Outline each Plasmodium ovale-infected red blood cell.
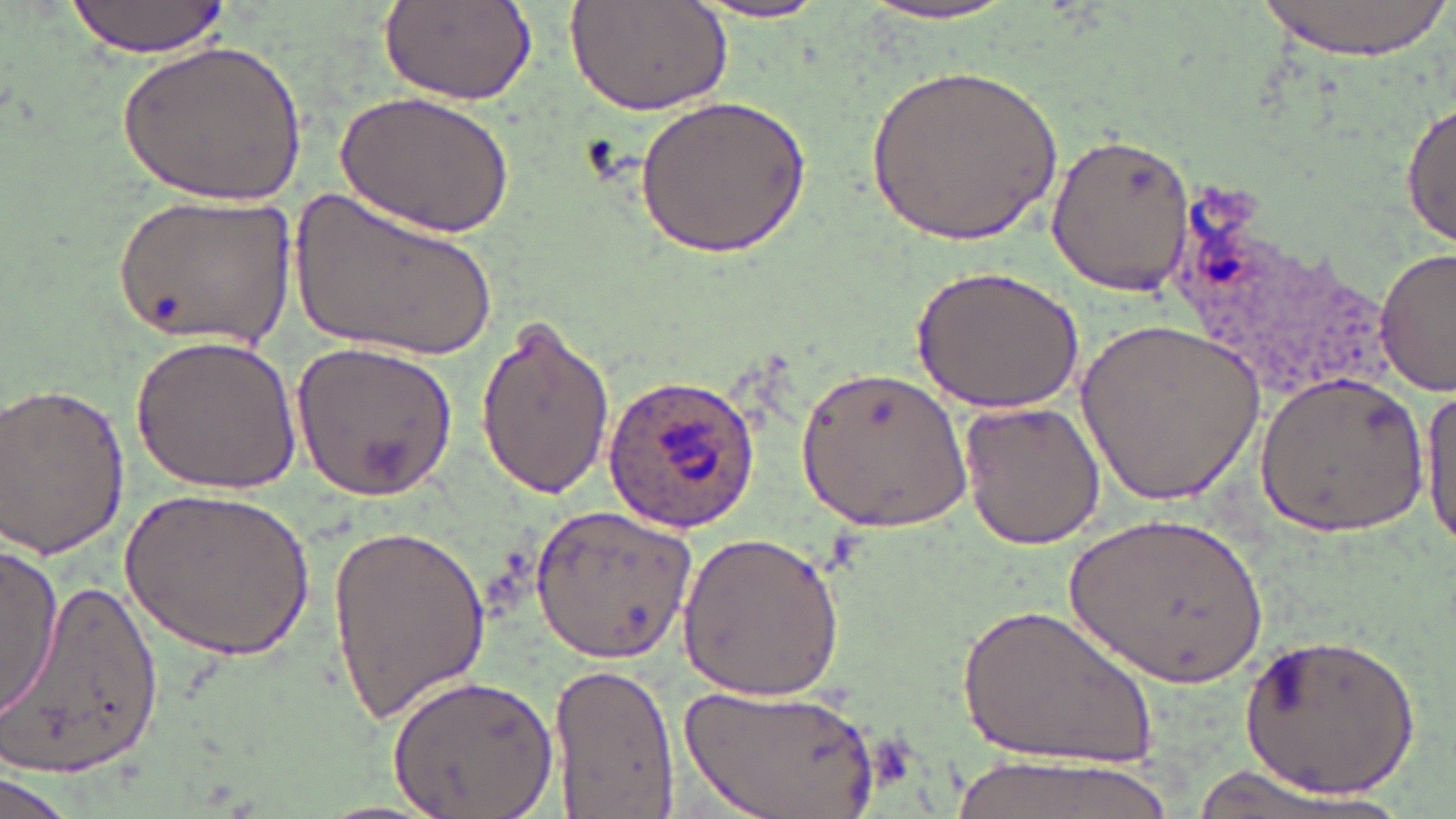

Approximate bounding boxes as (x1,y1)-(x2,y2) corner pairs in pixels.
Plasmodium ovale-infected red blood cells: (602,374)-(765,530).

{
  "slide_level_diagnosis": "Plasmodium ovale",
  "image_size": "1456×819 pixels",
  "field_of_view": "one of a larger specimen",
  "magnification": "1000x",
  "modality": "optical microscopy",
  "stain": "May-Grünwald-Giemsa",
  "uninfected_red_blood_cell_locations": "approximate bounding boxes as (x1,y1)-(x2,y2) corner pairs in pixels: (1253,0)-(1449,60), (63,1)-(230,58), (376,1)-(538,107), (567,1)-(733,115), (682,1)-(843,25), (849,3)-(1029,30), (124,39)-(310,205), (867,59)-(1063,248), (338,89)-(514,237), (635,95)-(814,260), (1400,101)-(1454,251), (1046,134)-(1198,296), (299,184)-(503,361), (112,194)-(295,349), (1376,248)-(1454,396), (913,264)-(1085,411), (474,315)-(617,498), (1074,315)-(1268,508), (130,334)-(306,496), (290,341)-(457,498), (798,362)-(971,532), (1251,367)-(1428,538), (2,380)-(133,561), (1419,385)-(1456,554), (960,397)-(1103,550), (123,483)-(313,664), (529,504)-(699,664), (1061,511)-(1270,689), (324,517)-(492,722), (675,532)-(849,699), (0,543)-(62,719), (5,572)-(162,780), (960,599)-(1157,774), (1237,628)-(1424,798), (549,660)-(677,819), (387,672)-(559,819), (681,684)-(882,819), (939,754)-(1176,819), (1169,767)-(1413,819), (0,773)-(74,819)",
  "preparation": "thin blood smear"
}